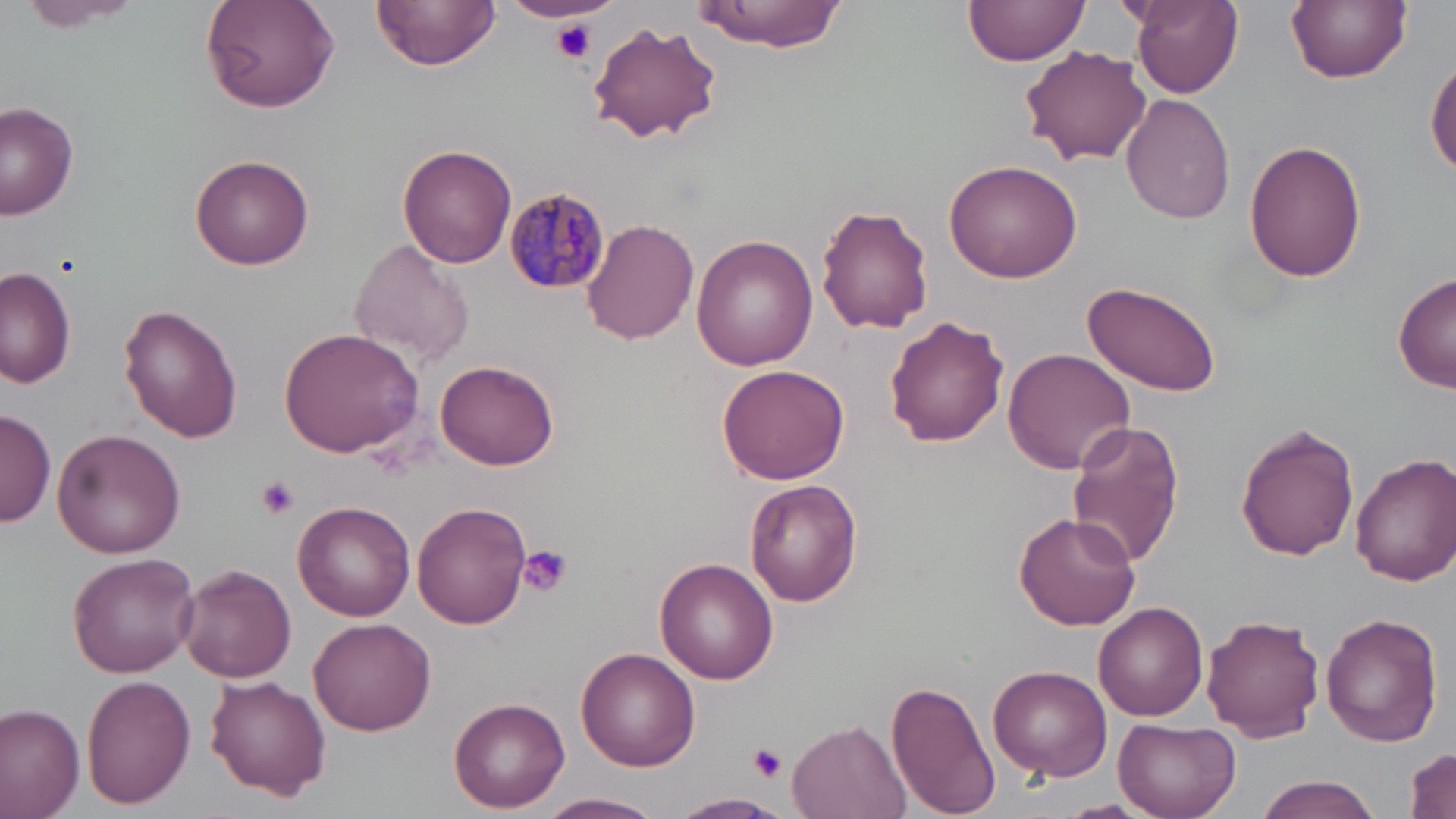 Approximate bounding boxes as [x1, y1, x2, y2] in pixels. Uninfected red blood cell locations: [372, 0, 498, 72], [963, 0, 1092, 71], [1130, 0, 1242, 97], [1287, 0, 1410, 84], [20, 1, 148, 34], [199, 1, 339, 113], [689, 1, 851, 50], [587, 21, 723, 144], [1019, 44, 1151, 167], [1428, 55, 1456, 181], [1121, 95, 1235, 225], [0, 104, 78, 220], [1243, 138, 1367, 283], [399, 145, 518, 267], [190, 154, 314, 271], [943, 158, 1082, 284], [817, 204, 935, 334], [583, 219, 699, 344], [691, 237, 820, 372], [347, 239, 474, 369], [0, 265, 78, 391], [1394, 271, 1456, 393], [1081, 280, 1223, 397], [120, 304, 244, 441], [884, 316, 1011, 447], [277, 328, 424, 458], [1002, 348, 1135, 473], [436, 359, 560, 470], [717, 363, 849, 485], [0, 410, 56, 528], [1064, 420, 1186, 569], [1236, 425, 1361, 560], [54, 430, 184, 555], [1351, 452, 1456, 585], [745, 480, 863, 607], [293, 500, 417, 621], [412, 500, 531, 630], [1014, 512, 1140, 630], [67, 552, 201, 678], [654, 557, 778, 683], [176, 563, 298, 683], [1094, 602, 1210, 720], [1320, 611, 1443, 747], [1203, 612, 1327, 742], [309, 617, 435, 734], [577, 647, 700, 771], [987, 665, 1112, 782], [80, 675, 196, 809], [205, 675, 330, 800], [887, 676, 997, 817], [448, 696, 570, 811], [0, 703, 85, 819], [786, 716, 911, 819], [1114, 717, 1241, 818], [1407, 747, 1454, 819], [1254, 775, 1382, 819], [543, 792, 663, 818], [671, 793, 789, 817], [1057, 797, 1151, 817]. Plasmodium malariae-infected red blood cell locations: [503, 186, 610, 292]. Platelet locations: [551, 21, 596, 63], [254, 475, 301, 519], [515, 544, 574, 596], [748, 743, 786, 782]. Slide-level diagnosis: Plasmodium malariae. May-Grünwald-Giemsa stain. Optical microscopy. Single field of view. Thin blood film. 1000x magnification. Image is 1456×819 pixels.